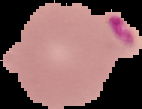

preparation = thin blood film
image type = cell region segmented out of the field of view; surrounding area masked to black
result = malaria parasites detected
image size = 142×109 pixels